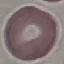
Malaria status: uninfected. Photographed with a smartphone camera at the microscope eyepiece. Automatically extracted cell patch, resized to 64 × 64 pixels. Giemsa-stained preparation. Thin smear of blood.